Report the malaria status of this cell.
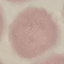
It is uninfected.

Summary:
  - Image type: automatically extracted cell patch, resized to 64 × 64 pixels
  - Stain: Giemsa
  - Preparation: thin smear
  - Capture: smartphone camera at the microscope eyepiece